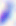
{
  "modality": "micrograph",
  "magnification": "400x",
  "identification": "Toxoplasma gondii"
}